Assess the morphology of the red blood cells.
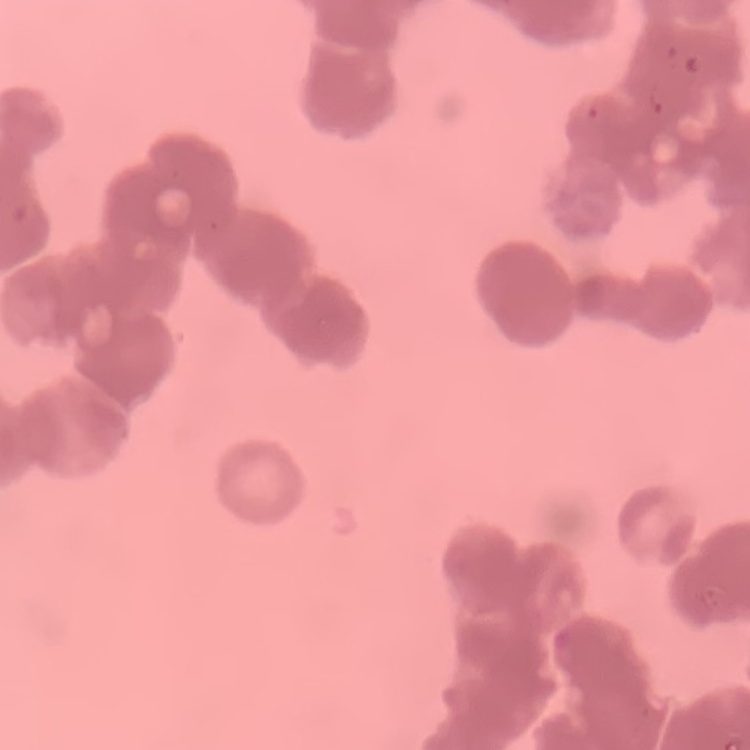

Rouleaux formation.

Square crop of a larger photomicrograph. Thin peripheral smear. Field's or Giemsa stain.